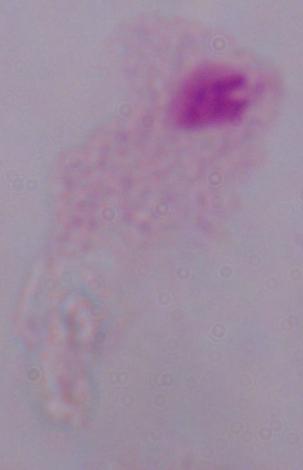

identification = trichomonad
magnification = 1000x
modality = micrograph